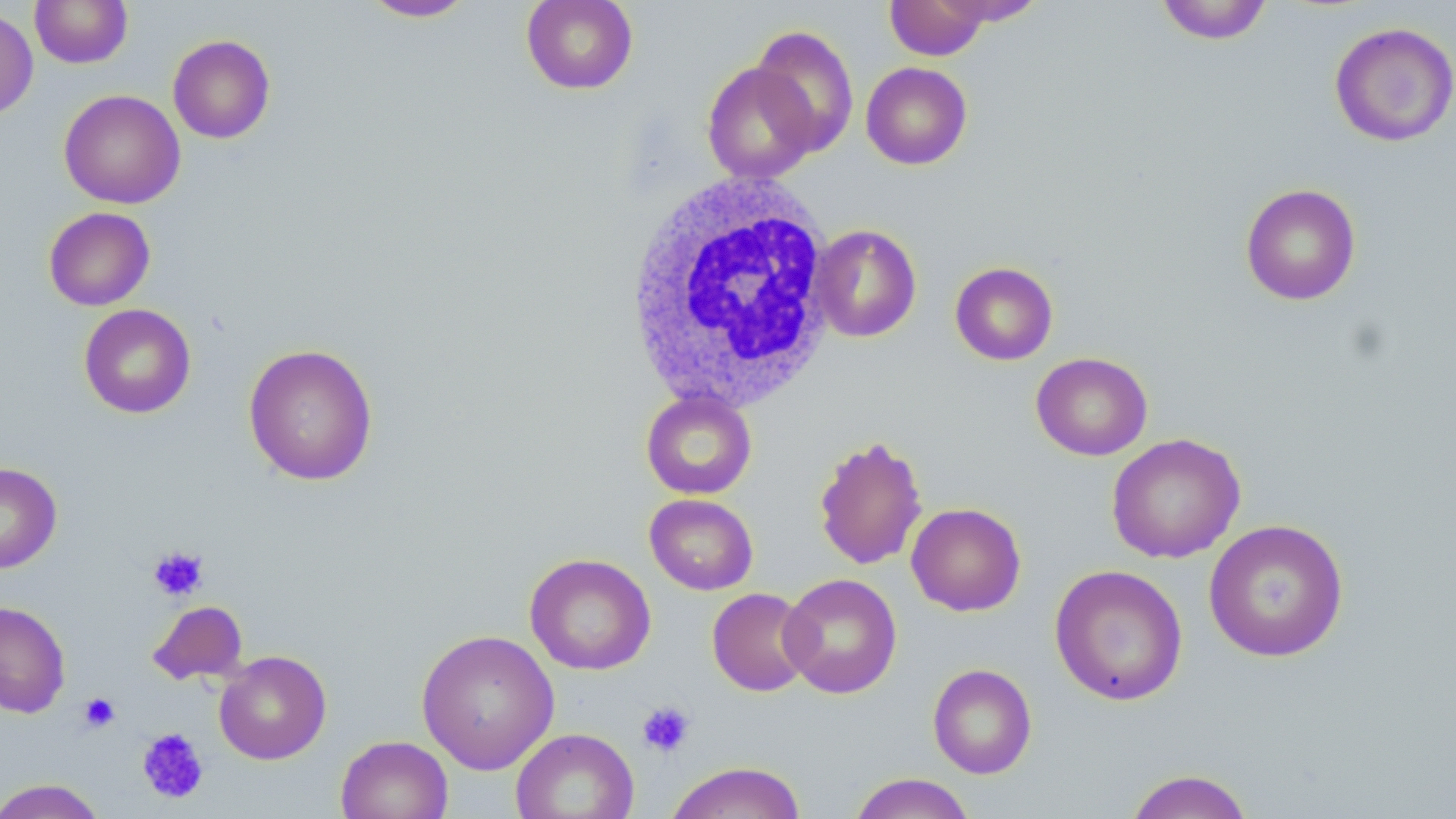

slide-level diagnosis = negative for blood parasites
stain = May-Grünwald-Giemsa
image size = 1456×819 pixels
uninfected red blood cell locations = approximate bounding boxes as [x1, y1, x2, y2] in pixels: [30, 0, 133, 68], [358, 0, 479, 22], [1155, 0, 1274, 44], [521, 1, 639, 94], [885, 1, 991, 60], [931, 1, 1047, 26], [0, 8, 38, 123], [1329, 21, 1456, 147], [750, 25, 859, 156], [167, 34, 276, 144], [702, 61, 819, 184], [861, 62, 972, 169], [59, 89, 185, 209], [1240, 183, 1361, 306], [43, 206, 156, 311], [810, 224, 922, 342], [950, 261, 1058, 365], [79, 304, 196, 419], [243, 343, 379, 486], [1031, 352, 1153, 460], [641, 390, 757, 500], [1106, 433, 1245, 563], [812, 434, 928, 571], [0, 462, 62, 573], [644, 493, 759, 595], [906, 502, 1026, 616], [1203, 518, 1349, 663], [525, 553, 656, 675], [1049, 564, 1188, 706], [779, 572, 903, 698], [707, 588, 815, 696], [0, 600, 71, 718], [147, 600, 248, 686], [416, 629, 560, 775], [213, 650, 331, 764], [927, 663, 1037, 779], [510, 728, 639, 819], [335, 734, 453, 819], [665, 761, 807, 819], [1123, 768, 1255, 819], [848, 772, 977, 819], [0, 778, 107, 819]
preparation = thin blood smear
white blood cell locations = approximate bounding boxes as [x1, y1, x2, y2] in pixels: [619, 169, 839, 414]
platelet locations = approximate bounding boxes as [x1, y1, x2, y2] in pixels: [147, 546, 208, 602], [78, 692, 121, 733], [636, 701, 695, 757], [136, 727, 210, 805]
field of view = single
magnification = 1000x
modality = light microscopy